Assess this cell for malaria.
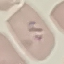

Parasitized.

capture: smartphone camera at the microscope eyepiece
stain: Giemsa
preparation: thin blood film
image_type: cell patch, automatically extracted from a larger field of view and resized to 64 × 64 pixels